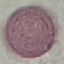
{
  "malaria_status": "uninfected",
  "preparation": "thin blood smear",
  "image_type": "automatically extracted cell patch, resized to 64 × 64 pixels",
  "stain": "Giemsa",
  "capture": "smartphone through the microscope eyepiece"
}